Classify this cell by malaria status.
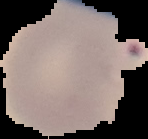

Parasitized.

Summary:
  - Preparation: thin blood film
  - Image type: segmented cell region with the area outside set to black
  - Image size: 148×139 pixels